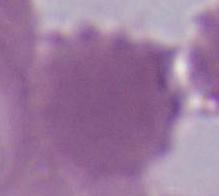

A red blood cell is shown. Captured at 1000x magnification. Micrograph.